State the blood parasite species.
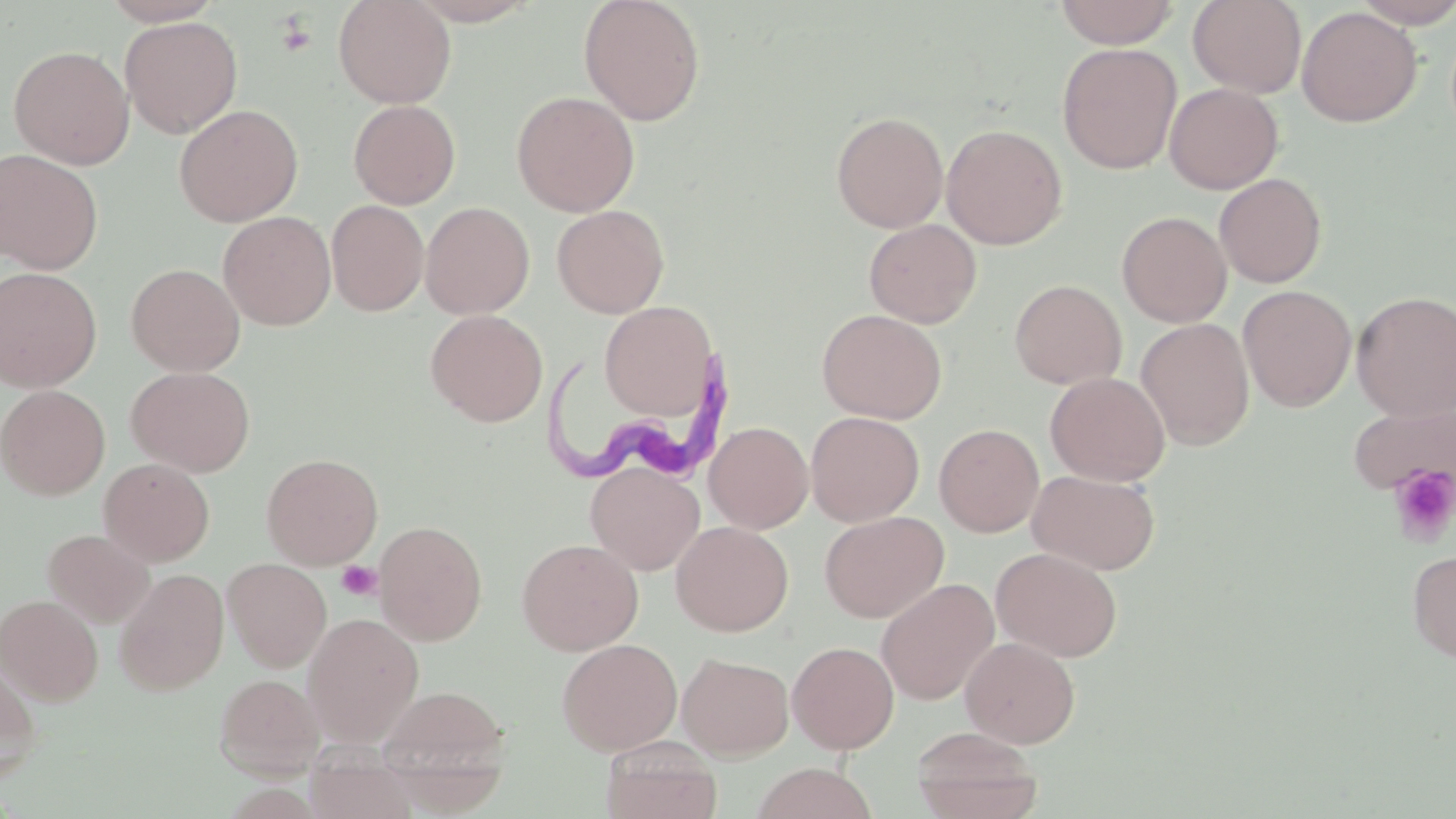
Trypanosoma brucei.

Approximate bounding boxes as [x1, y1, x2, y2] in pixels. Uninfected red blood cell locations: [101, 0, 224, 26], [333, 0, 457, 108], [406, 0, 540, 25], [578, 0, 706, 126], [1054, 0, 1181, 48], [1188, 0, 1307, 98], [1350, 0, 1456, 28], [1296, 6, 1422, 127], [120, 15, 242, 139], [1057, 43, 1182, 174], [8, 44, 134, 169], [1164, 83, 1283, 195], [511, 90, 640, 217], [349, 99, 461, 209], [173, 104, 303, 227], [831, 111, 949, 232], [941, 123, 1067, 249], [0, 149, 104, 274], [1214, 173, 1328, 288], [326, 199, 429, 316], [420, 201, 534, 319], [552, 204, 669, 318], [218, 211, 337, 331], [1117, 211, 1232, 327], [863, 219, 982, 328], [126, 263, 245, 376], [0, 266, 103, 393], [1009, 279, 1126, 389], [1238, 285, 1357, 412], [1352, 291, 1456, 420], [599, 301, 718, 420], [817, 308, 947, 424], [425, 309, 548, 426], [1135, 318, 1255, 450], [126, 366, 255, 477], [1045, 372, 1170, 486], [0, 385, 110, 500], [1347, 400, 1456, 496], [806, 411, 924, 526], [704, 421, 813, 534], [934, 423, 1044, 537], [261, 453, 383, 569], [99, 458, 215, 567], [586, 462, 704, 576], [1027, 469, 1160, 575], [819, 511, 948, 623], [374, 520, 488, 646], [671, 520, 793, 637], [42, 529, 154, 628], [517, 538, 643, 655], [991, 547, 1123, 662], [1407, 549, 1456, 664], [222, 557, 332, 671], [114, 568, 229, 695], [876, 578, 999, 705], [0, 594, 103, 705], [302, 613, 424, 747], [960, 636, 1080, 748], [557, 638, 682, 756], [787, 641, 899, 753], [677, 652, 794, 760], [0, 653, 42, 782], [214, 673, 325, 779], [376, 684, 512, 792], [911, 726, 1042, 819], [601, 737, 721, 819], [750, 762, 878, 819]. Platelet locations: [274, 15, 317, 58], [1389, 463, 1456, 547], [336, 561, 381, 601]. Trypanosoma brucei locations: [539, 346, 747, 489]. One field of a larger specimen. Thin blood smear. May-Grünwald-Giemsa stain. Optical microscopy. Image is 1456×819 pixels. 1000x magnification.